State which cell type is depicted.
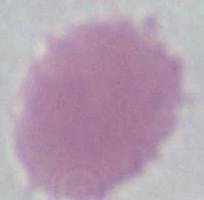

An erythrocyte.

modality: photomicrograph
magnification: 1000x